Comment on the morphology of the erythrocytes.
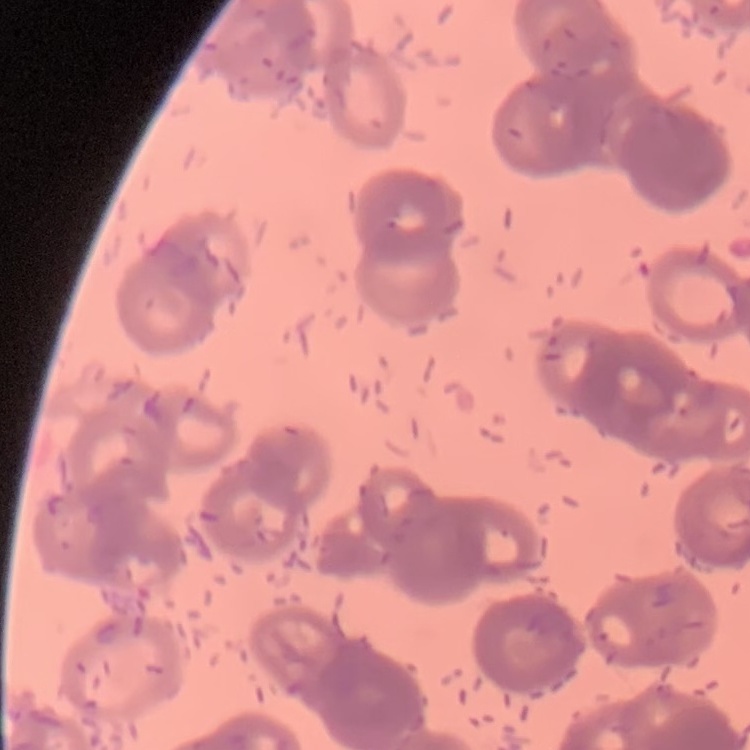

They show rouleaux formation.

Thin blood smear. Field's or Giemsa stain. Square crop of a larger photomicrograph.